Comment on the morphology of the erythrocytes.
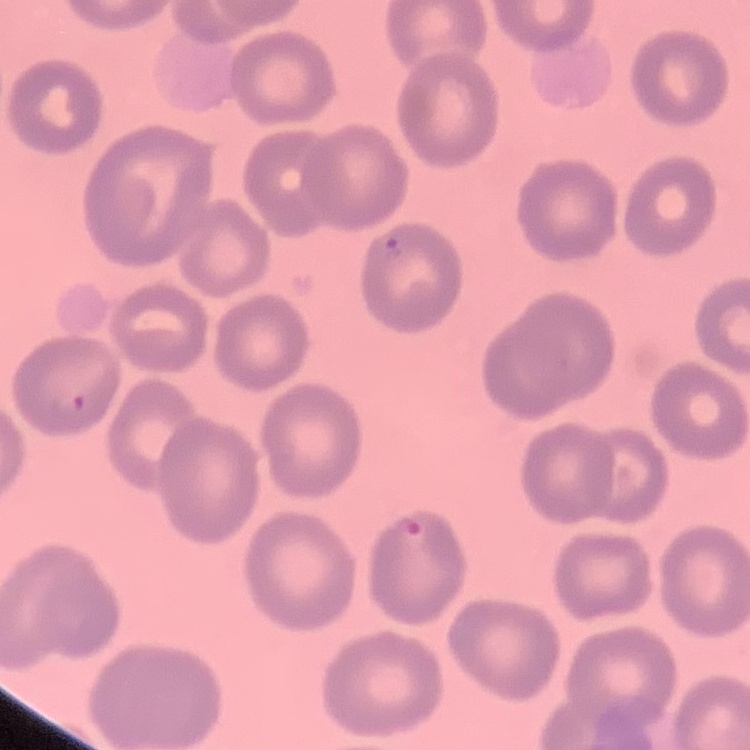
They show no rouleaux formation.

Square crop of a larger photomicrograph. Thin blood smear. Stained with either Field's or Giemsa.